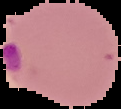

Summary:
  - Malaria status: parasitized
  - Image type: segmented cell region with the area outside set to black
  - Preparation: thin blood film
  - Image size: 121×109 pixels